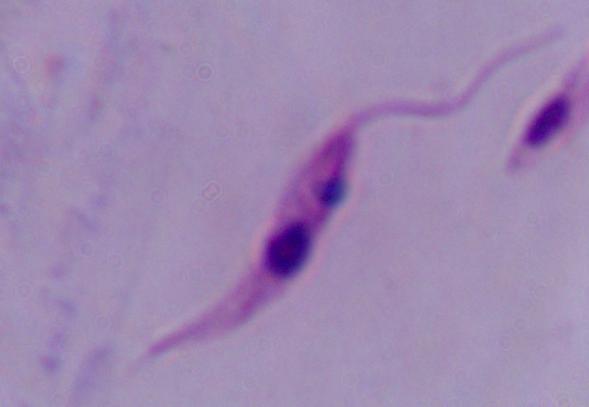
Summary:
  - Modality: photomicrograph
  - Identification: Leishmania
  - Magnification: 1000x